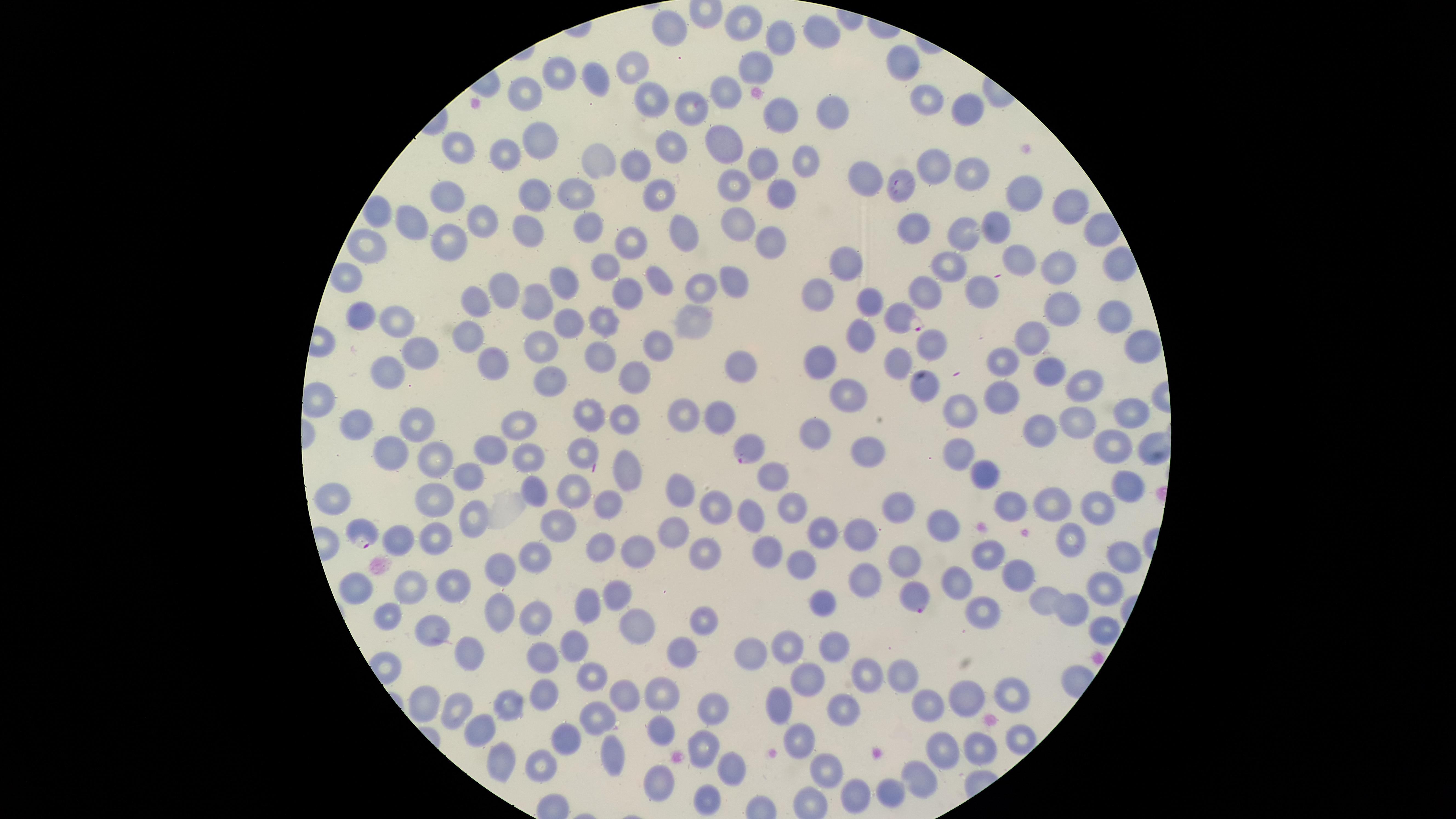

Approximate marker points as (x, y) in pixels.
Summary:
  - Parasitized RBCs: (898, 186), (900, 319), (743, 448), (362, 534), (916, 596)
  - Uninfected RBCs: (745, 26), (668, 27), (819, 33), (777, 37), (900, 63), (752, 68), (629, 71), (555, 72), (597, 76), (722, 90), (518, 94), (652, 98), (928, 101), (691, 104), (821, 111), (968, 112), (776, 115), (531, 141), (669, 144), (726, 145), (457, 146), (508, 152), (600, 157), (801, 161), (926, 165), (634, 167), (761, 167), (966, 172), (869, 184), (731, 187), (779, 192), (1019, 192), (660, 193), (528, 194), (447, 195), (576, 195), (1065, 204), (376, 216), (482, 219), (409, 222), (726, 222), (593, 225), (993, 226), (919, 230), (528, 231), (966, 234), (680, 235), (629, 241), (769, 242), (364, 246), (447, 246), (1020, 256), (843, 263), (949, 263), (603, 265), (1111, 267), (1052, 271), (347, 276), (730, 279), (659, 280), (500, 286), (706, 287), (561, 292), (978, 292), (926, 293), (817, 294), (616, 297), (532, 300), (873, 301), (469, 303), (1058, 310), (364, 314), (1109, 316), (691, 317), (395, 320), (600, 322), (569, 324), (861, 331), (462, 339), (1033, 340), (654, 342), (540, 344), (927, 344), (1134, 345), (416, 352), (601, 357), (1003, 360), (486, 361), (820, 362), (895, 363), (734, 365), (385, 366), (1045, 370), (546, 377), (635, 378), (1087, 378), (928, 379), (844, 393), (1000, 397), (678, 412), (964, 412), (1129, 412), (622, 416), (714, 417), (582, 418), (356, 422), (420, 422), (1077, 422), (521, 424), (817, 426), (1040, 429), (1114, 444), (863, 448), (485, 450), (524, 452), (579, 452), (391, 453), (949, 453), (433, 463), (988, 468), (627, 469), (773, 473), (469, 474), (1127, 485), (570, 488), (681, 488), (338, 494), (431, 499), (1055, 500), (603, 501), (1009, 503), (1098, 504), (788, 507), (897, 507), (713, 511), (752, 513), (471, 519), (554, 523), (943, 529), (823, 531), (669, 532), (861, 532), (400, 538), (431, 539), (599, 544), (634, 544), (535, 547), (765, 547), (703, 551), (989, 555), (1122, 555), (904, 557), (798, 565), (498, 569), (1015, 576), (865, 577), (956, 578), (355, 584), (409, 585), (458, 586), (1099, 590), (615, 592), (1042, 596), (587, 602), (821, 603), (980, 607), (534, 608), (390, 609), (1074, 611), (497, 612), (702, 621), (629, 625), (430, 627), (1097, 630), (785, 645), (574, 646), (683, 646), (830, 647), (748, 652), (471, 655), (541, 656), (864, 671), (592, 675), (901, 675), (812, 677), (535, 692), (615, 695), (1008, 696), (654, 697), (422, 698), (508, 700), (777, 700), (959, 705), (456, 706), (842, 706), (929, 709), (711, 710), (592, 720), (477, 721), (658, 733), (799, 736), (569, 738), (1017, 740), (705, 745), (976, 749), (940, 750), (613, 752), (497, 760), (535, 760), (724, 768), (913, 774), (821, 775), (660, 782), (889, 794), (709, 799)
  - Visible region: circular
  - Preparation: thin smear of blood
  - Image size: 1456×819 pixels
  - Species: Plasmodium falciparum
  - Stain: Giemsa
  - Presence: malaria parasites seen
  - Capture: smartphone photograph through the microscope eyepiece
  - Field of view: single